Locate and identify every blood parasite.
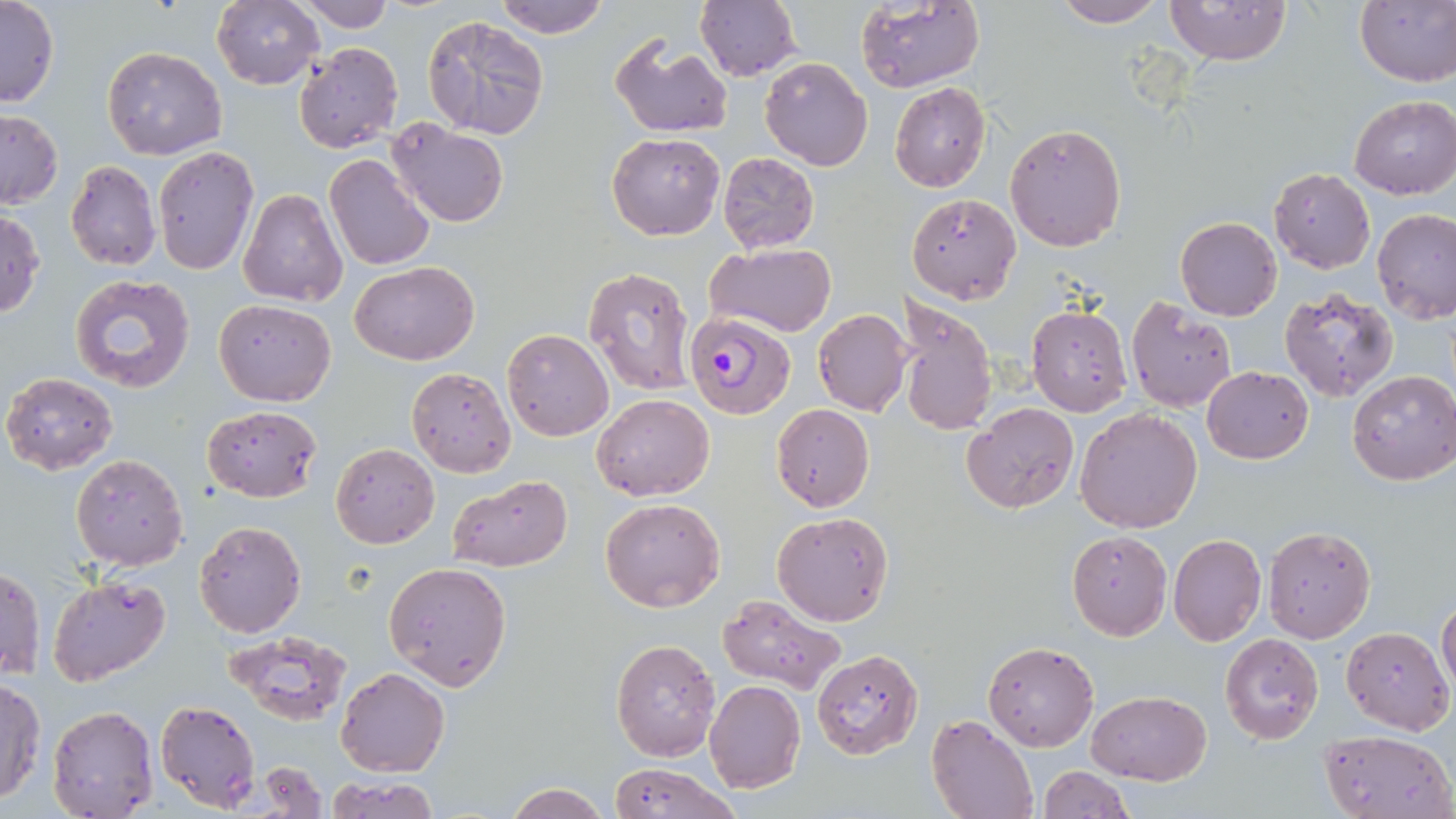
Approximate bounding boxes as (x1,y1)-(x2,y2) corner pairs in pixels.
Plasmodium falciparum-infected red blood cells: (684,311)-(796,420).
No Plasmodium ovale, Plasmodium malariae, Plasmodium vivax, Babesia divergens, or Trypanosoma brucei observed.

Summary:
  - Uninfected red blood cell locations: (294,0)-(395,32), (491,0)-(612,40), (1052,0)-(1167,27), (1166,0)-(1291,68), (1354,0)-(1456,86), (0,1)-(59,108), (211,1)-(324,89), (855,1)-(984,93), (694,2)-(802,81), (421,14)-(550,140), (609,36)-(732,138), (294,42)-(403,154), (102,46)-(227,160), (759,57)-(872,171), (890,82)-(991,193), (1348,96)-(1456,201), (0,109)-(62,208), (387,119)-(507,228), (1004,122)-(1127,251), (607,132)-(725,240), (152,145)-(260,277), (717,151)-(820,253), (323,154)-(435,271), (64,159)-(161,270), (1270,168)-(1375,273), (239,189)-(347,308), (908,193)-(1020,304), (0,208)-(46,320), (1374,211)-(1456,325), (1175,217)-(1282,321), (705,243)-(837,338), (350,261)-(477,366), (582,266)-(697,397), (70,274)-(196,392), (1279,287)-(1400,403), (895,296)-(998,436), (214,299)-(336,406), (1126,299)-(1237,412), (1027,306)-(1131,417), (812,308)-(910,416), (500,328)-(613,441), (1202,366)-(1314,464), (406,367)-(515,477), (1,370)-(119,474), (1347,370)-(1456,486), (592,393)-(714,501), (961,402)-(1078,514), (772,403)-(874,512), (201,404)-(323,502), (1075,408)-(1203,532), (331,443)-(439,549), (71,453)-(189,570), (446,474)-(573,572), (600,497)-(726,612), (771,510)-(895,628), (194,521)-(306,638), (1262,526)-(1375,642), (1066,531)-(1171,640), (1167,534)-(1265,647), (382,560)-(512,690), (2,565)-(44,680), (47,577)-(171,685), (719,595)-(846,694), (1437,597)-(1456,697), (1340,625)-(1453,733), (223,630)-(352,724), (1220,631)-(1325,744), (610,635)-(722,760), (984,641)-(1098,750), (810,648)-(926,760), (337,667)-(450,777), (1,679)-(47,805), (703,681)-(806,795), (1086,690)-(1211,784), (154,699)-(260,815), (47,705)-(158,818), (926,715)-(1038,819), (1322,728)-(1455,819), (251,763)-(328,815), (609,763)-(740,819), (1037,766)-(1134,819), (327,774)-(440,819), (504,781)-(610,818)
  - Slide-level diagnosis: Plasmodium falciparum
  - Image size: 1456×819 pixels
  - Stain: May-Grünwald-Giemsa
  - Preparation: thin blood smear
  - Field of view: one of a larger specimen
  - Modality: light microscopy
  - Magnification: 1000x